Point out every malaria parasite and every leukocyte.
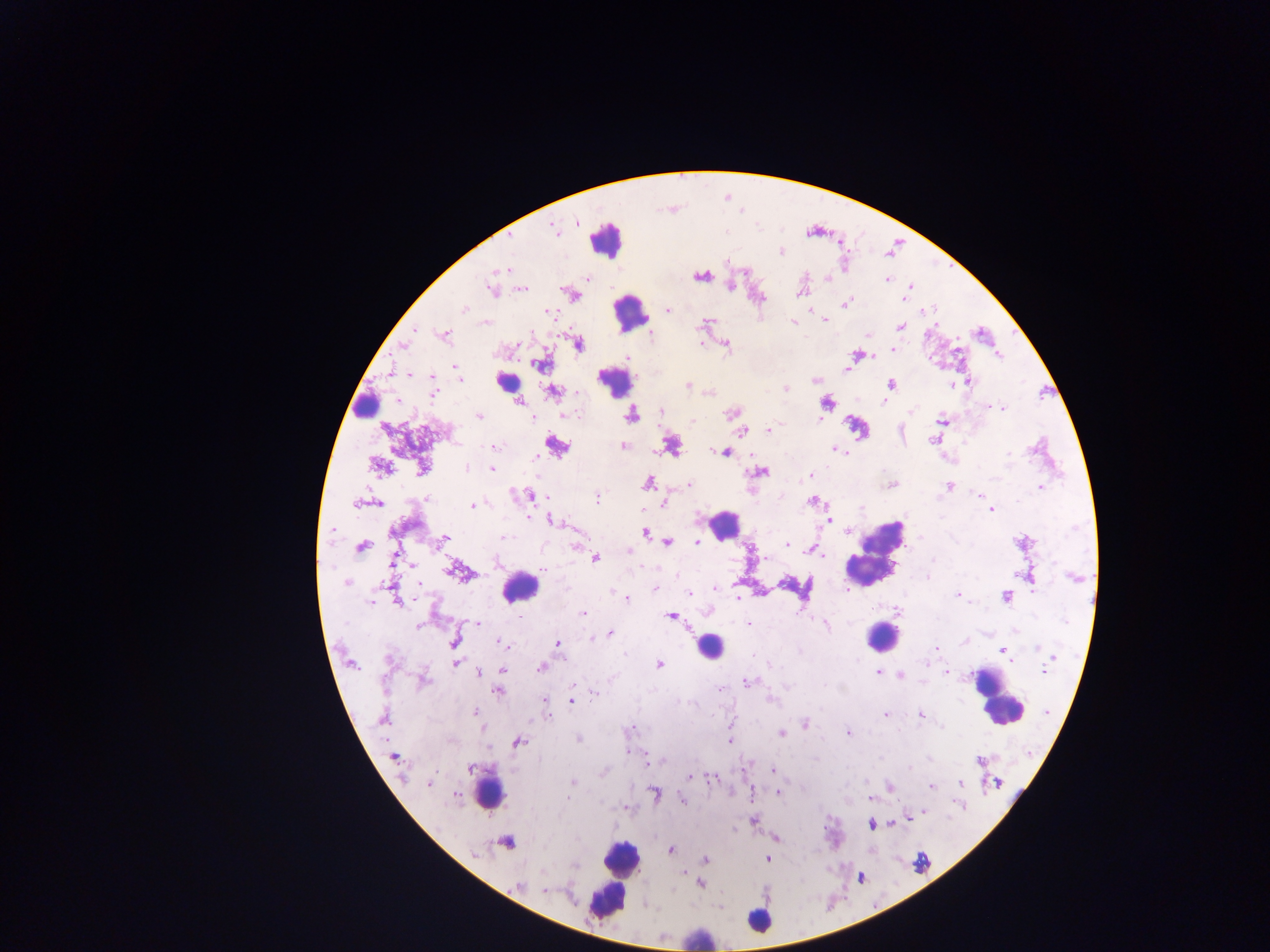
Approximate centers as (x, y) in pixels.
Malaria parasites: (577, 222), (554, 230), (781, 252), (727, 260), (502, 269), (699, 276), (587, 278), (826, 278), (887, 279), (910, 286), (730, 287), (491, 288), (523, 289), (799, 293), (905, 298), (846, 303), (464, 309), (667, 311), (549, 312), (825, 320), (793, 322), (707, 323), (901, 326), (415, 329), (531, 333), (444, 335), (651, 335), (868, 335), (578, 344), (403, 345), (726, 345), (893, 349), (627, 357), (540, 365), (455, 367), (847, 369), (458, 373), (409, 375), (815, 380), (432, 381), (968, 382), (891, 384), (952, 384), (688, 385), (786, 388), (552, 391), (433, 392), (709, 393), (884, 402), (518, 403), (826, 403), (989, 406), (1003, 409), (661, 411), (912, 411), (731, 413), (569, 415), (632, 415), (479, 416), (576, 416), (533, 418), (819, 418), (941, 419), (691, 421), (768, 430), (742, 432), (933, 441), (495, 446), (623, 446), (671, 447), (836, 449), (725, 452), (1008, 453), (535, 458), (379, 466), (421, 467), (466, 468), (491, 469), (761, 472), (811, 475), (648, 482), (689, 484), (891, 485), (950, 486), (1040, 487), (977, 493), (529, 495), (427, 498), (597, 499), (811, 501), (664, 503), (356, 504), (378, 504), (471, 506), (862, 508), (991, 510), (528, 517), (829, 520), (552, 521), (332, 531), (848, 531), (645, 533), (445, 537), (504, 537), (441, 542), (697, 542), (668, 543), (577, 546), (787, 546), (790, 546), (362, 547), (811, 549), (629, 551), (765, 557), (393, 559), (595, 559), (933, 560), (411, 564), (456, 572), (927, 577), (1073, 578), (347, 583), (389, 584), (417, 585), (655, 588), (716, 588), (1032, 592), (688, 593), (958, 595), (1005, 596), (738, 598), (626, 599), (370, 602), (399, 602), (897, 610), (583, 613), (670, 616), (477, 623), (749, 624), (417, 625), (826, 626), (610, 634), (602, 635), (592, 638), (454, 641), (501, 643), (557, 643), (936, 648), (1038, 648), (1003, 651), (1053, 657), (389, 659), (456, 662), (925, 663), (658, 664), (771, 666), (541, 668), (504, 670), (1043, 671), (878, 672), (946, 672), (479, 673), (901, 675), (423, 680), (746, 682), (574, 687), (721, 689), (498, 691), (595, 694), (771, 699), (544, 700), (571, 701), (474, 711), (1046, 712), (884, 715), (921, 715), (549, 716), (382, 720), (805, 724), (942, 727), (631, 728), (780, 733), (848, 733), (578, 739), (729, 742), (517, 743), (628, 751), (394, 758), (979, 761), (648, 762), (471, 768), (909, 768), (772, 770), (603, 772), (690, 776), (712, 778), (573, 782), (960, 783), (997, 783), (429, 784), (890, 787), (931, 787), (778, 793), (457, 794), (570, 794), (653, 794), (568, 798), (870, 799), (682, 800), (926, 812), (908, 819), (753, 820), (892, 823), (871, 825), (776, 839), (507, 843), (671, 849), (475, 855), (767, 858), (705, 859), (574, 865), (700, 883), (519, 886), (544, 890).
Leukocytes: (606, 238), (630, 312), (502, 382), (615, 382), (366, 401), (557, 446), (722, 525), (875, 553), (520, 587), (880, 636), (709, 647), (996, 699), (489, 791), (616, 876), (608, 897), (758, 921), (699, 937).

Photographed through a microscope with a mobile-phone camera. Thick blood film. One field of view. Image is 1270×952 pixels. Sample from Ghana.